Locate white blood cells.
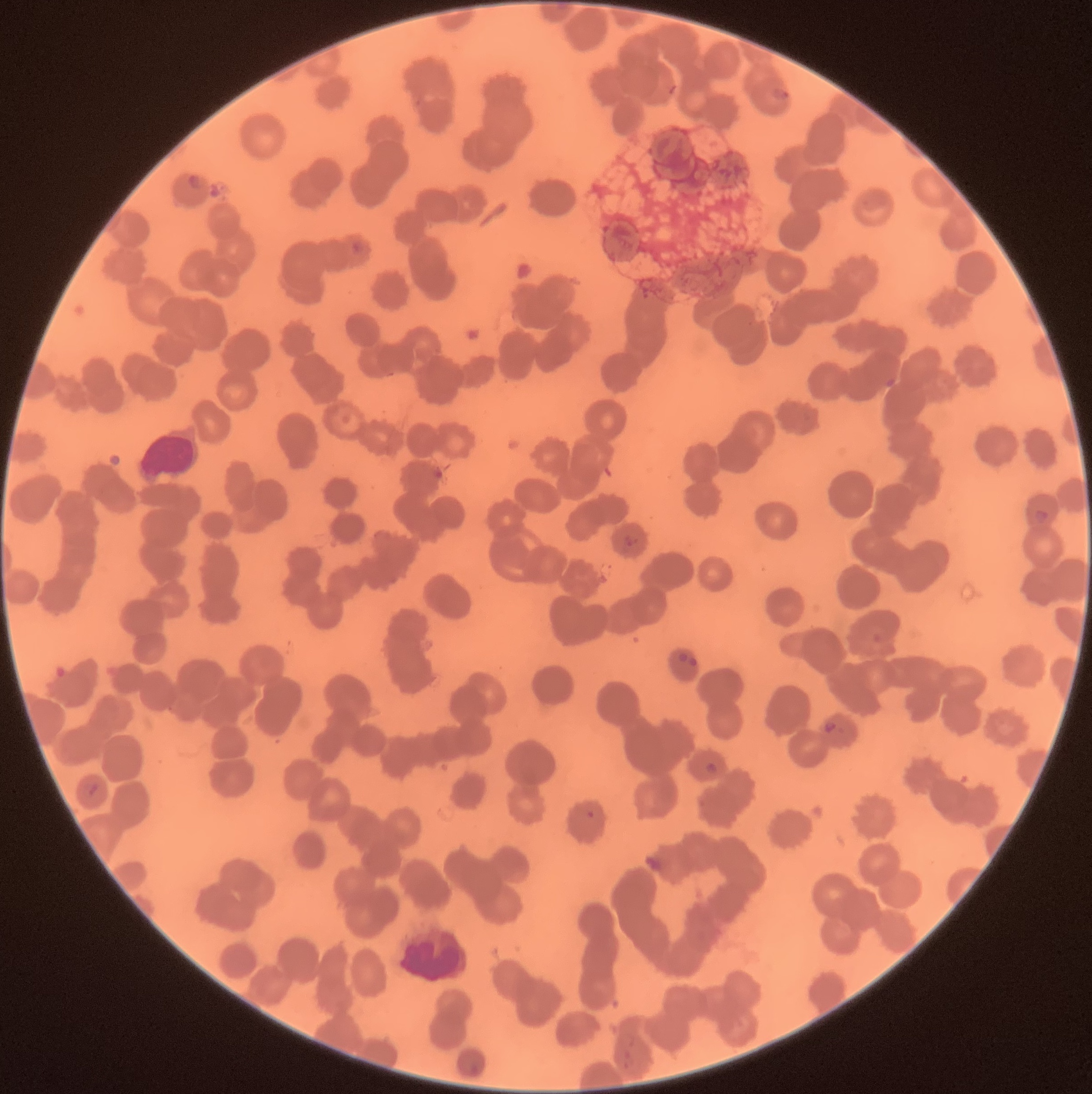

Approximate bounding boxes as (x1,y1)-(x2,y2) corner pairs in pixels.
White blood cells: (133,428)-(209,485).

Plasmodium parasite locations: (769,86)-(794,104), (186,174)-(206,191), (349,241)-(367,255), (881,377)-(901,388), (431,466)-(446,482), (1033,507)-(1049,524), (622,534)-(639,549), (678,651)-(700,669), (823,721)-(839,733), (704,762)-(717,775), (83,781)-(99,796), (586,810)-(596,820), (642,853)-(669,875). The red blood cells show rouleaux formation. Thin blood smear. Image is 1092×1094 pixels. Optical microscopy.